Outline each blood parasite and name the species.
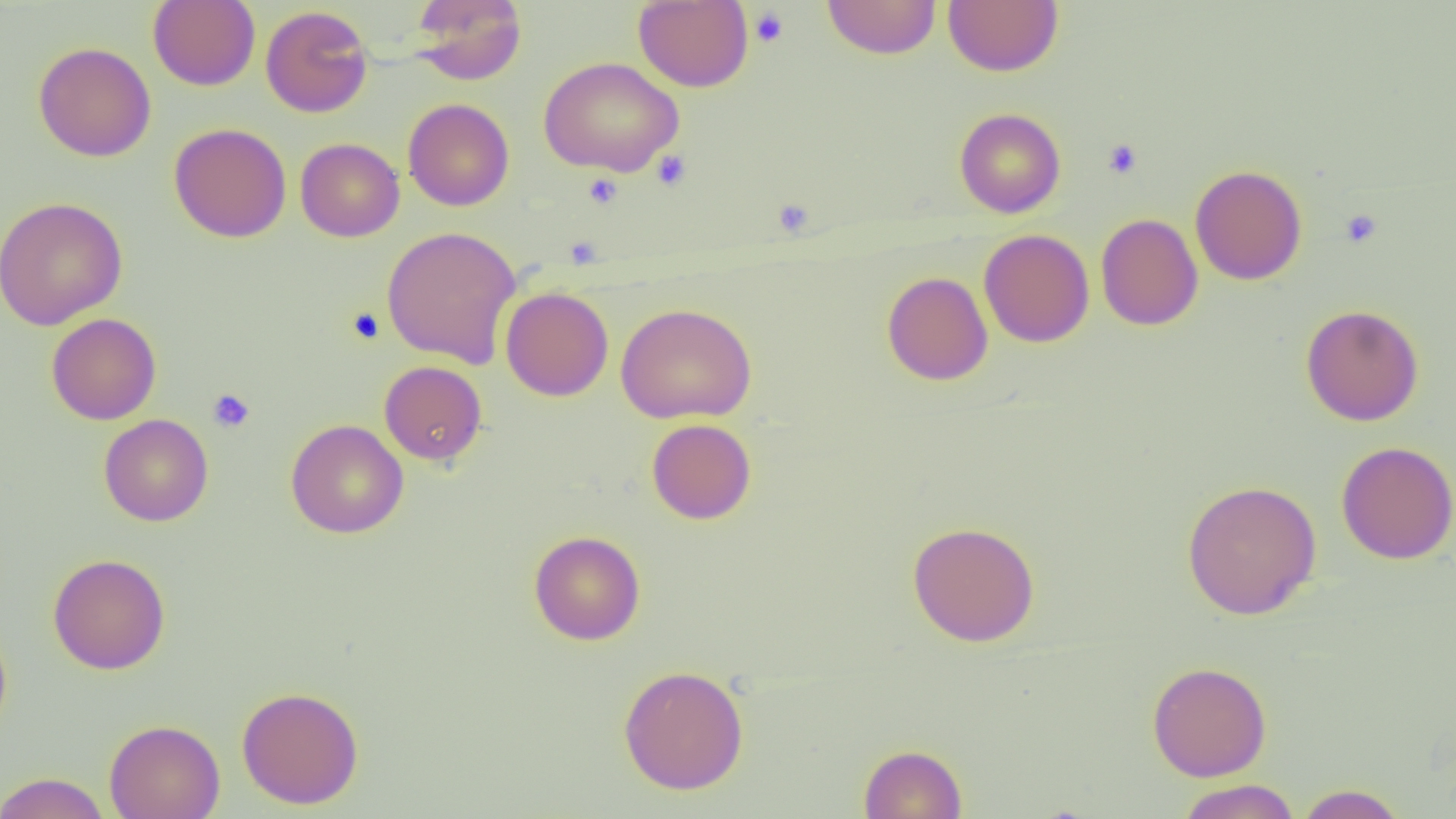
No blood parasites seen.

Summary:
  - Coordinate format: approximate bounding boxes as (x1,y1)-(x2,y2) corner pairs in pixels
  - Platelet locations: (749,7)-(789,48), (1102,139)-(1143,179), (651,150)-(692,191), (583,173)-(623,209), (772,198)-(815,237), (1340,209)-(1382,248), (346,307)-(384,344), (208,388)-(255,433)
  - Uninfected red blood cell locations: (148,0)-(260,90), (409,0)-(526,85), (822,0)-(941,59), (943,0)-(1063,76), (633,1)-(753,91), (260,5)-(373,118), (33,42)-(156,161), (539,57)-(683,176), (403,98)-(514,211), (954,108)-(1066,218), (169,122)-(292,243), (295,138)-(404,242), (1190,165)-(1308,285), (0,196)-(128,330), (1095,213)-(1203,330), (382,225)-(521,368), (978,229)-(1094,348), (881,271)-(993,386), (500,287)-(614,401), (615,303)-(756,424), (1300,304)-(1424,426), (47,312)-(162,425), (379,361)-(487,466), (98,414)-(214,527), (646,418)-(757,524), (285,419)-(409,539), (1335,441)-(1456,565), (1182,478)-(1322,620), (907,520)-(1040,647), (528,530)-(645,645), (47,553)-(170,674), (0,621)-(13,741), (1147,661)-(1272,781), (618,664)-(749,795), (236,685)-(365,809), (104,718)-(225,819), (858,744)-(967,819), (0,772)-(111,818), (1176,779)-(1301,819), (1295,784)-(1408,818)
  - Slide-level diagnosis: no evidence of blood parasites
  - Preparation: thin blood film
  - Image size: 1456×819 pixels
  - Modality: optical microscopy
  - Magnification: 1000x
  - Field of view: single